Report the malaria status of this cell.
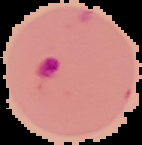
Parasitized.

From a thin blood smear. Cell region segmented out of the field of view; the surrounding area is masked to black. Image is 142×145 pixels.